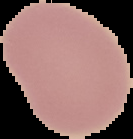

Summary:
  - Preparation: thin blood film
  - Image size: 133×139 pixels
  - Result: negative for Plasmodium parasites
  - Image type: segmented cell region on a black background